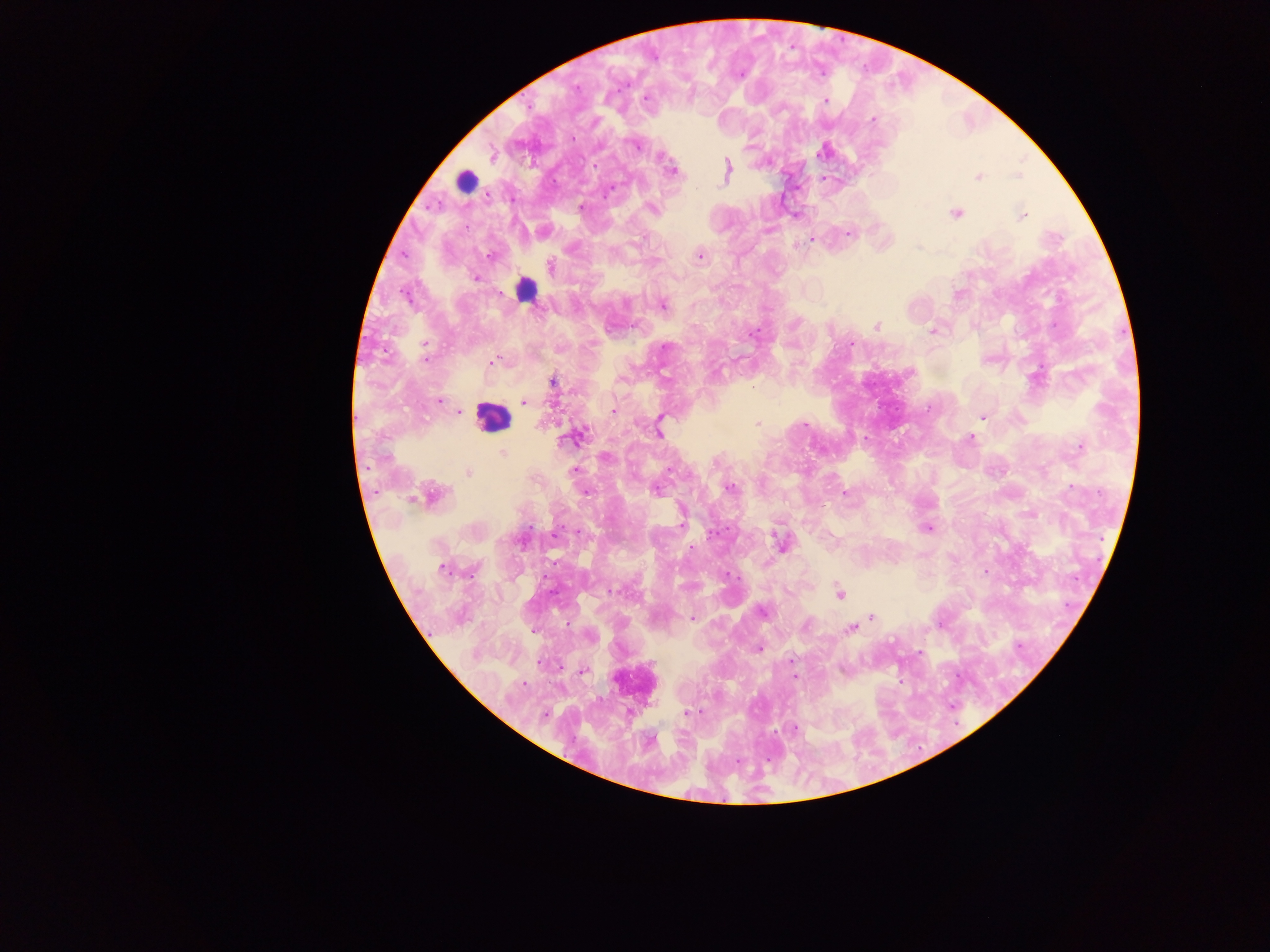 Approximate centers as x y in pixels. Leukocyte locations: 465 181; 525 290; 492 417; 633 682. Plasmodium parasite locations: 576 87; 645 97; 825 101; 872 119; 635 145; 492 155; 660 157; 595 165; 673 171; 727 171; 1018 176; 978 177; 581 206; 652 209; 955 212; 1022 215; 849 234; 811 240; 489 256; 700 256; 550 266; 475 278; 663 305; 877 325; 932 332; 753 333; 851 344; 664 346; 425 347; 425 358; 493 361; 553 382; 753 387; 439 401; 523 402; 613 411; 458 412; 982 417; 660 419; 757 423; 659 431; 570 439; 970 439; 1079 447; 503 452; 606 456; 670 469; 573 470; 468 473; 1071 486; 729 488; 655 490; 586 493; 845 493; 433 495; 413 498; 681 523; 927 528; 713 533; 781 544; 442 569; 985 573; 727 574; 613 591; 840 594; 762 611; 871 618; 692 619; 850 629; 534 632; 759 649; 919 653; 583 671; 794 677; 688 712; 545 714; 795 728. Mobile-phone photograph taken through the microscope. Collected in Ghana. One field of view. Thick blood smear. Image is 1270×952 pixels.